Assess this cell for malaria.
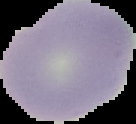
Uninfected.

Summary:
  - Preparation: thin blood film
  - Image size: 136×124 pixels
  - Image type: cell region segmented out of the field of view; surrounding area masked to black